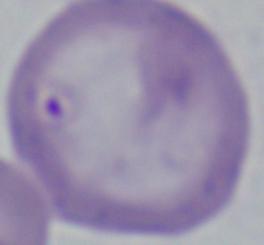
modality = photomicrograph
identification = Babesia
magnification = 1000x